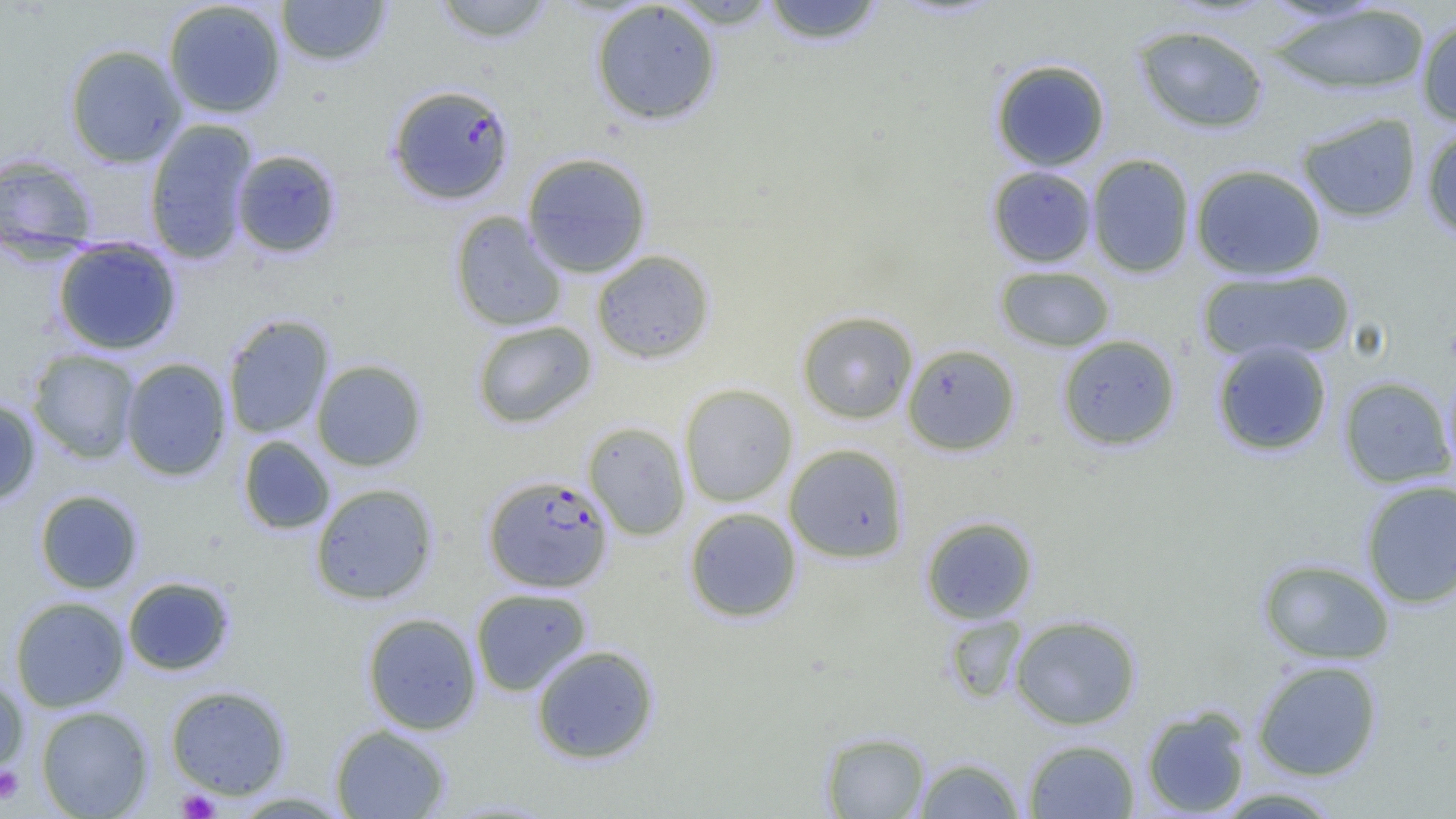
Approximate bounding boxes as (x1, y1, x2, y2) in pixels. Plasmodium falciparum-infected red blood cell locations: (387, 83, 515, 205), (483, 473, 613, 592). Platelet locations: (0, 765, 24, 805), (177, 789, 220, 818). Uninfected red blood cell locations: (275, 0, 391, 67), (430, 0, 558, 44), (664, 0, 783, 29), (759, 0, 888, 45), (163, 1, 287, 119), (590, 1, 722, 126), (1267, 3, 1432, 97), (1416, 16, 1456, 127), (1133, 24, 1269, 133), (64, 43, 187, 167), (990, 59, 1111, 172), (1296, 112, 1421, 223), (144, 118, 258, 265), (1421, 124, 1456, 241), (230, 149, 343, 258), (521, 151, 652, 278), (0, 153, 98, 258), (1086, 153, 1195, 278), (1190, 163, 1327, 280), (987, 165, 1097, 268), (450, 211, 568, 332), (52, 237, 183, 355), (591, 249, 715, 364), (995, 266, 1116, 352), (1198, 268, 1355, 364), (796, 311, 918, 423), (222, 314, 334, 439), (472, 320, 597, 428), (1057, 334, 1181, 450), (1212, 341, 1333, 456), (902, 343, 1021, 455), (27, 349, 141, 464), (120, 358, 232, 481), (311, 359, 427, 471), (1338, 376, 1455, 488), (679, 383, 798, 507), (0, 397, 42, 507), (582, 421, 691, 540), (238, 435, 335, 534), (784, 444, 909, 563), (1360, 479, 1456, 609), (310, 483, 438, 605), (34, 489, 143, 594), (684, 507, 802, 622), (920, 515, 1038, 624), (1257, 557, 1395, 665), (122, 576, 235, 675), (470, 587, 591, 696), (10, 595, 130, 712), (362, 612, 482, 735), (1010, 614, 1142, 730), (943, 615, 1027, 704), (530, 644, 659, 764), (1252, 660, 1383, 781), (0, 671, 29, 779), (165, 685, 292, 800), (1141, 704, 1252, 817), (35, 705, 153, 818), (330, 724, 451, 818), (820, 730, 931, 818), (1023, 739, 1139, 818), (914, 756, 1025, 818), (1212, 787, 1346, 818), (229, 792, 352, 817). Slide-level diagnosis: Plasmodium falciparum. Light microscopy. Thin blood smear. One field of a larger specimen. Captured at 1000x magnification. Image is 1456×819 pixels.